Report the malaria status of this cell.
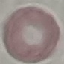

It is uninfected.

{
  "preparation": "thin smear",
  "capture": "smartphone camera at the microscope eyepiece",
  "stain": "Giemsa",
  "image_type": "cell patch, automatically extracted from a larger field of view and resized to 64 × 64 pixels"
}